Assess this cell for malaria.
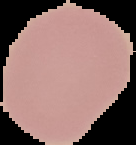

Uninfected.

image_type: cell region segmented out of the field of view; surrounding area masked to black
image_size: 136×145 pixels
preparation: thin blood film